Locate every blood parasite and identify its species.
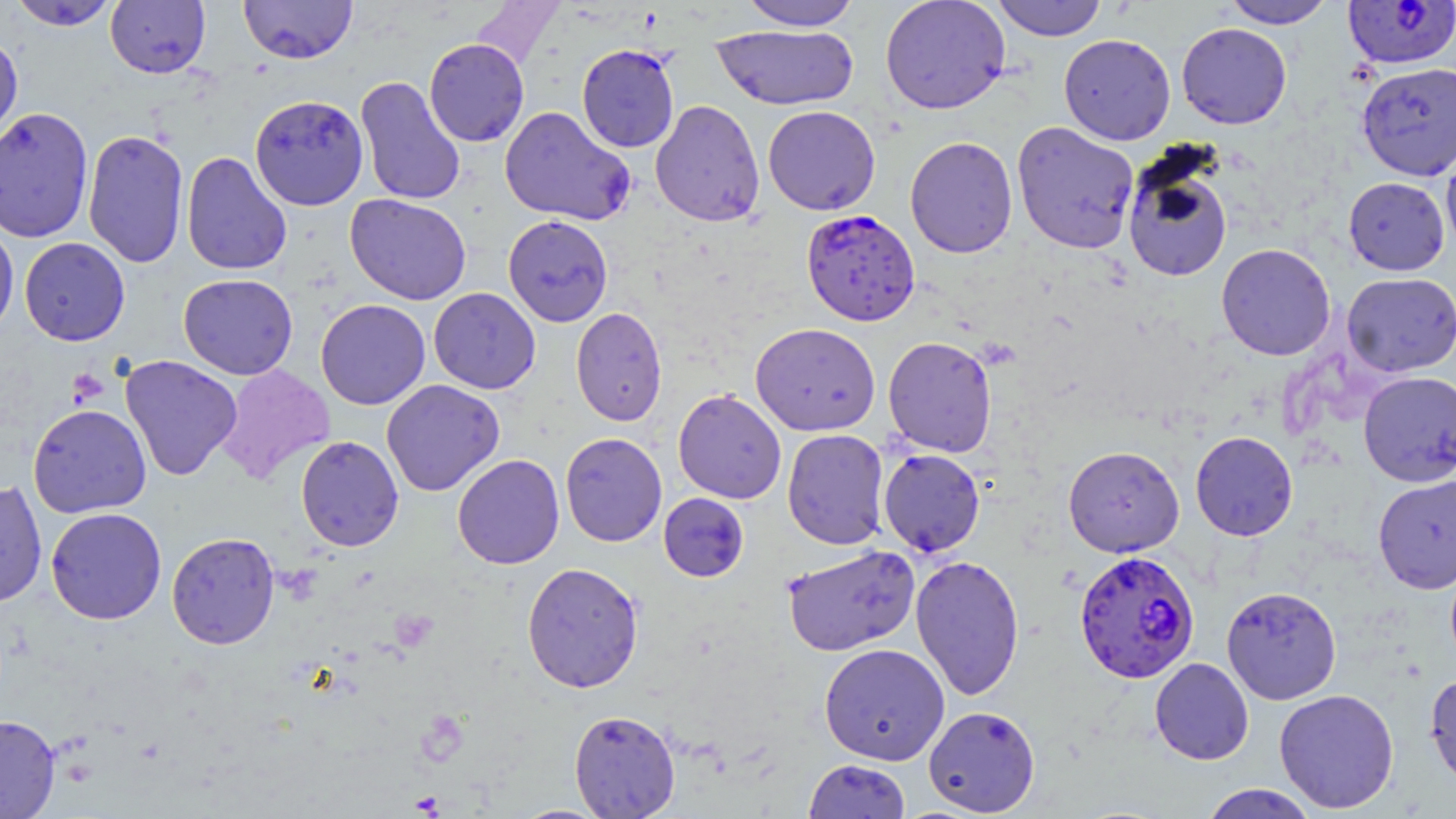
Approximate bounding boxes as named x1/y1/x2/y2 corners in pixels.
Plasmodium falciparum-infected red blood cells: (x1=1342, y1=1, x2=1456, y2=70), (x1=801, y1=208, x2=920, y2=326), (x1=1073, y1=549, x2=1200, y2=684).
No Plasmodium ovale, Plasmodium malariae, Plasmodium vivax, Babesia divergens, or Trypanosoma brucei observed.

Platelet locations: (x1=67, y1=368, x2=108, y2=405). Uninfected red blood cell locations: (x1=7, y1=0, x2=121, y2=31), (x1=105, y1=0, x2=211, y2=78), (x1=239, y1=0, x2=357, y2=64), (x1=739, y1=0, x2=861, y2=31), (x1=880, y1=0, x2=1011, y2=115), (x1=992, y1=0, x2=1107, y2=41), (x1=1220, y1=0, x2=1337, y2=28), (x1=471, y1=1, x2=563, y2=72), (x1=1176, y1=22, x2=1292, y2=129), (x1=711, y1=25, x2=859, y2=110), (x1=0, y1=31, x2=23, y2=149), (x1=1058, y1=33, x2=1176, y2=145), (x1=424, y1=38, x2=529, y2=147), (x1=576, y1=44, x2=680, y2=153), (x1=1356, y1=62, x2=1456, y2=181), (x1=354, y1=75, x2=466, y2=206), (x1=249, y1=94, x2=369, y2=210), (x1=649, y1=99, x2=765, y2=226), (x1=499, y1=105, x2=635, y2=226), (x1=762, y1=105, x2=881, y2=215), (x1=0, y1=107, x2=93, y2=243), (x1=1011, y1=121, x2=1140, y2=254), (x1=82, y1=128, x2=189, y2=269), (x1=904, y1=136, x2=1018, y2=258), (x1=1441, y1=142, x2=1456, y2=258), (x1=181, y1=151, x2=292, y2=275), (x1=1121, y1=152, x2=1234, y2=283), (x1=1343, y1=176, x2=1451, y2=276), (x1=345, y1=193, x2=472, y2=305), (x1=503, y1=214, x2=613, y2=326), (x1=0, y1=219, x2=19, y2=343), (x1=19, y1=237, x2=130, y2=346), (x1=1216, y1=243, x2=1336, y2=361), (x1=1341, y1=272, x2=1456, y2=377), (x1=178, y1=273, x2=298, y2=380), (x1=428, y1=287, x2=541, y2=394), (x1=316, y1=299, x2=430, y2=410), (x1=571, y1=307, x2=667, y2=426), (x1=750, y1=322, x2=880, y2=436), (x1=883, y1=335, x2=998, y2=457), (x1=120, y1=354, x2=242, y2=480), (x1=215, y1=364, x2=335, y2=485), (x1=1358, y1=370, x2=1456, y2=487), (x1=381, y1=379, x2=504, y2=497), (x1=672, y1=388, x2=787, y2=504), (x1=27, y1=403, x2=151, y2=518), (x1=782, y1=428, x2=890, y2=550), (x1=1190, y1=431, x2=1298, y2=541), (x1=560, y1=432, x2=667, y2=547), (x1=295, y1=435, x2=404, y2=551), (x1=1062, y1=445, x2=1185, y2=557), (x1=877, y1=448, x2=986, y2=557), (x1=452, y1=454, x2=564, y2=569), (x1=1372, y1=474, x2=1456, y2=593), (x1=0, y1=480, x2=48, y2=609), (x1=658, y1=493, x2=749, y2=582), (x1=45, y1=507, x2=167, y2=624), (x1=166, y1=532, x2=279, y2=649), (x1=782, y1=544, x2=919, y2=656), (x1=910, y1=554, x2=1025, y2=700), (x1=521, y1=562, x2=644, y2=692), (x1=1221, y1=585, x2=1342, y2=704), (x1=819, y1=643, x2=950, y2=765), (x1=1149, y1=657, x2=1254, y2=765), (x1=1424, y1=670, x2=1456, y2=793), (x1=1273, y1=688, x2=1400, y2=813), (x1=923, y1=705, x2=1041, y2=816), (x1=569, y1=709, x2=680, y2=818), (x1=0, y1=714, x2=60, y2=818), (x1=803, y1=759, x2=911, y2=819), (x1=1199, y1=784, x2=1318, y2=819). Slide-level diagnosis: Plasmodium falciparum. Thin blood smear. Light microscopy. Single field of view. Captured at 1000x magnification. Image is 1456×819 pixels. May-Grünwald-Giemsa-stained preparation.